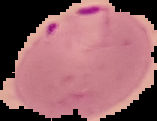
Image is 157×121 pixels. Malaria status: parasitized. The area outside the segmented cell region is set to black. From a thin blood smear.